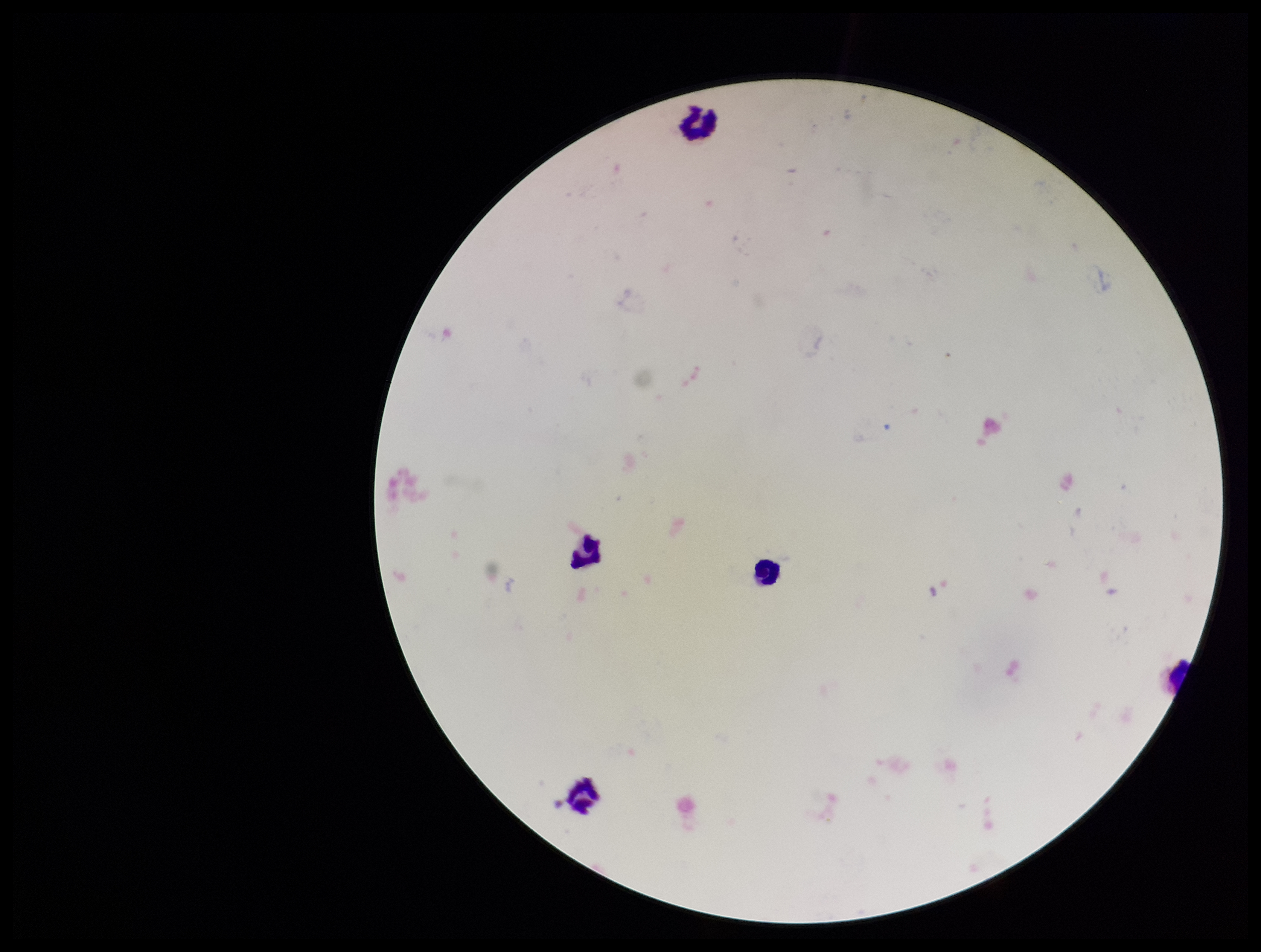
Summary:
  - Image size: 1261×952 pixels
  - Preparation: thick smear
  - Patient malaria status: negative
  - Plasmodium parasites: none detected
  - Field of view: single
  - Capture: smartphone photograph through the microscope eyepiece
  - Stain: Giemsa
  - Parasite count: 0
  - Leukocyte count: 4